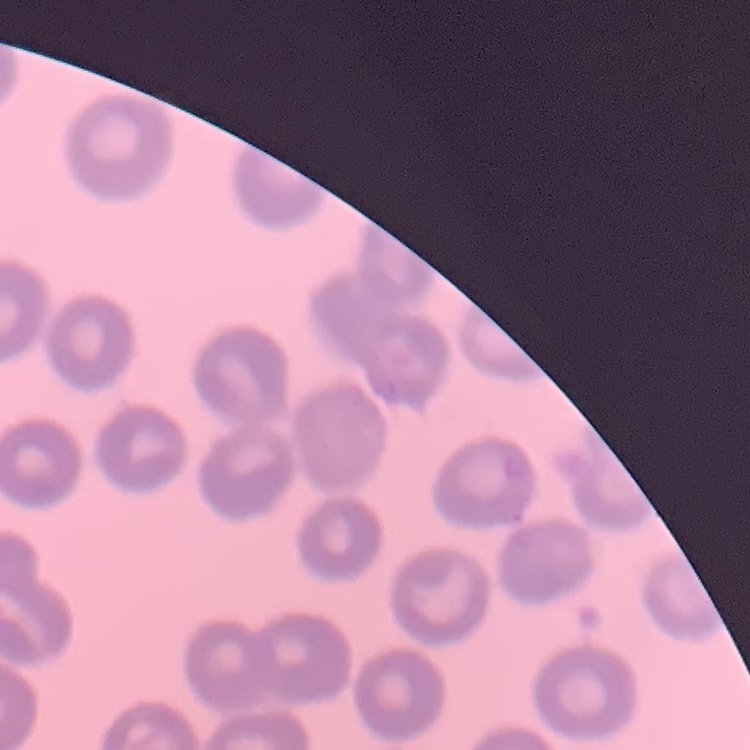

Summary:
  - Erythrocyte morphology: no rouleaux formation
  - Image type: square crop of a larger photomicrograph
  - Stain: Field's or Giemsa
  - Preparation: thin blood film